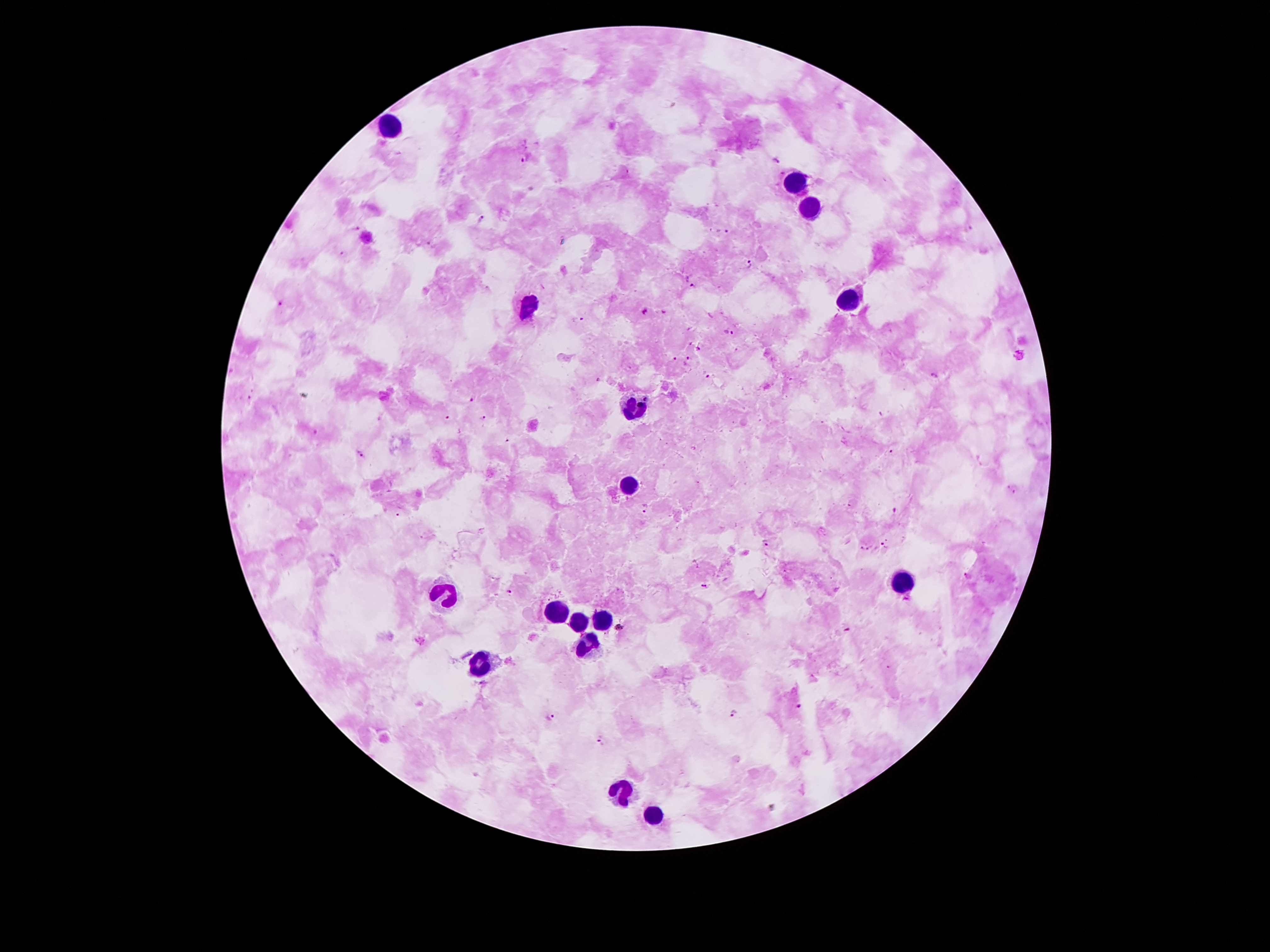

{
  "capture": "smartphone through the microscope eyepiece",
  "stain": "Giemsa",
  "field_of_view": "one from this slide",
  "magnification": "100x",
  "preparation": "thick peripheral-blood smear",
  "leukocyte_locations": "approximate object centers, in pixels from the top-left corner: (x=388, y=125), (x=798, y=177), (x=808, y=208), (x=850, y=301), (x=524, y=308), (x=633, y=404), (x=625, y=483), (x=902, y=583), (x=447, y=593), (x=554, y=608), (x=601, y=617), (x=578, y=620), (x=586, y=642), (x=480, y=662), (x=623, y=788), (x=653, y=815)",
  "patient_malaria_status": "positive for Plasmodium falciparum",
  "image_size": "1270×952 pixels",
  "malaria_parasite_locations": "approximate object centers, in pixels from the top-left corner: (x=526, y=157), (x=778, y=162), (x=481, y=219), (x=356, y=228), (x=727, y=231), (x=751, y=266), (x=692, y=285), (x=281, y=302), (x=645, y=312), (x=664, y=313), (x=581, y=320), (x=729, y=333), (x=699, y=348), (x=675, y=358), (x=687, y=361), (x=706, y=373), (x=933, y=375), (x=473, y=402), (x=484, y=417), (x=447, y=418), (x=891, y=451), (x=361, y=454), (x=1015, y=490), (x=646, y=508), (x=894, y=511), (x=768, y=540), (x=886, y=542), (x=861, y=547), (x=869, y=547), (x=968, y=576), (x=702, y=586), (x=508, y=591), (x=618, y=626), (x=847, y=630), (x=799, y=705), (x=734, y=711), (x=550, y=715), (x=601, y=740)"
}